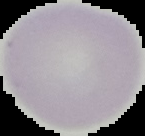
Malaria status: uninfected. From a thin blood smear. Image is 145×136 pixels. The area outside the segmented cell region is set to black.